Locate and identify every blood parasite.
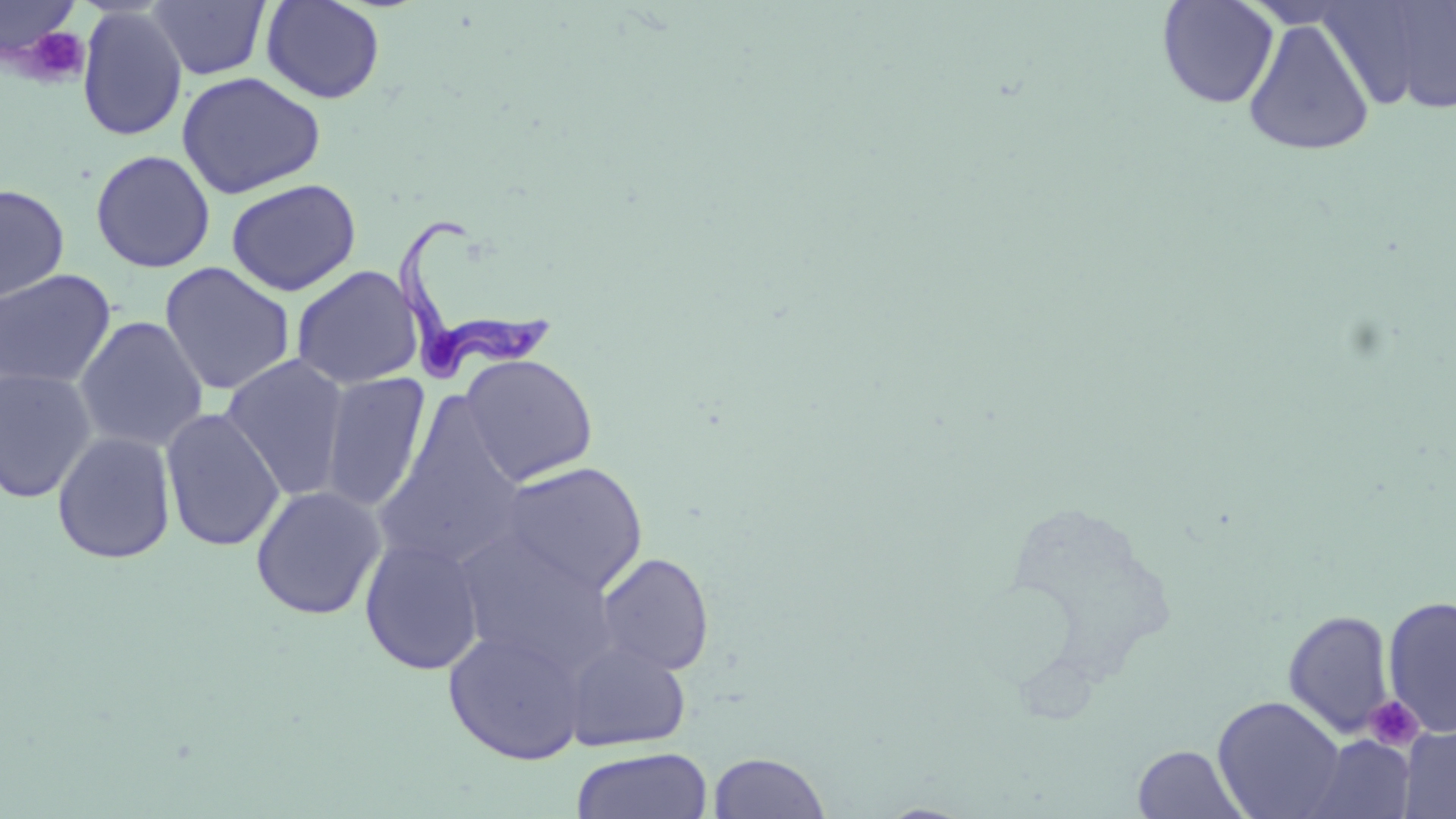

Approximate bounding boxes as (x1,y1)-(x2,y2) corner pairs in pixels.
Trypanosoma brucei: (395,223)-(563,382).
No Plasmodium falciparum, Plasmodium ovale, Plasmodium malariae, Plasmodium vivax, or Babesia divergens observed.

Uninfected red blood cell locations: (0,0)-(84,64), (261,0)-(385,104), (1157,0)-(1279,110), (1323,0)-(1456,116), (147,1)-(271,81), (77,7)-(188,142), (1241,17)-(1377,157), (177,71)-(326,199), (89,149)-(215,273), (225,178)-(362,296), (0,184)-(70,303), (159,262)-(295,396), (290,265)-(423,390), (0,269)-(117,391), (73,316)-(209,453), (460,353)-(599,486), (219,354)-(352,501), (0,368)-(98,503), (320,371)-(431,513), (374,397)-(527,571), (160,407)-(286,553), (51,431)-(177,565), (498,461)-(649,598), (250,485)-(386,620), (453,531)-(619,674), (358,536)-(486,675), (596,551)-(715,676), (1382,595)-(1456,738), (1282,609)-(1395,739), (442,628)-(589,765), (562,640)-(692,751), (1212,696)-(1347,819), (1399,724)-(1456,819), (1304,734)-(1415,819), (1132,744)-(1249,819), (571,747)-(712,819), (708,752)-(832,818). Platelet locations: (16,22)-(90,86), (1363,695)-(1425,751). Slide-level diagnosis: Trypanosoma brucei. Optical microscopy. Single field of view. Thin blood smear. May-Grünwald-Giemsa stain. Image is 1456×819 pixels. Captured at 1000x magnification.